Classify this cell by malaria status.
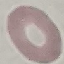
Uninfected.

Acquired by smartphone through the microscope eyepiece. Giemsa stain. Cell patch, automatically extracted from a larger field of view and resized to 64 × 64 pixels. Thin smear of blood.